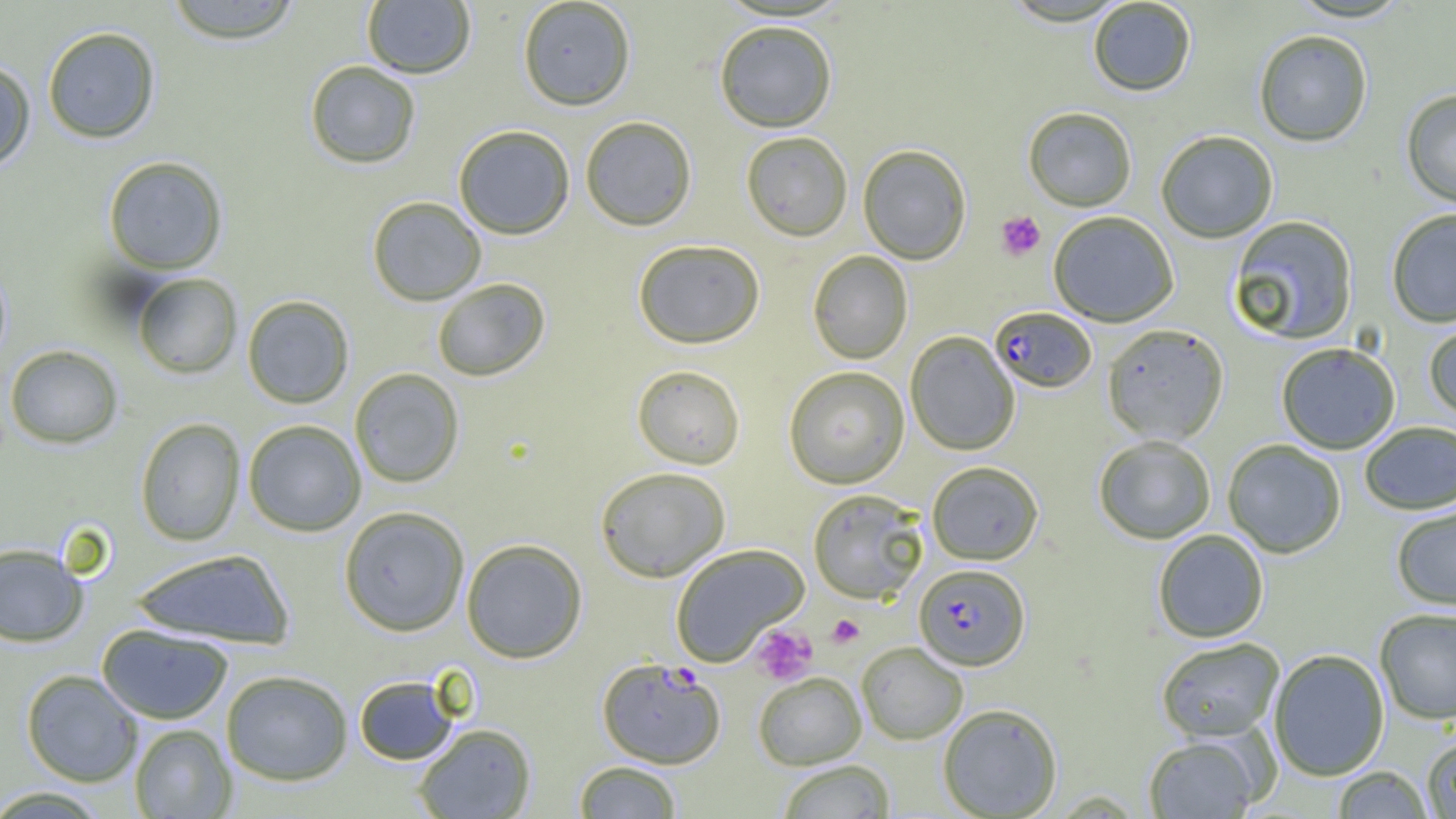

slide_level_diagnosis: Plasmodium falciparum
magnification: 1000x
field_of_view: one of a larger specimen
platelet_locations: 'approximate bounding boxes as (x1, y1, x2, y2) in pixels: (996, 211, 1045, 261), (827, 614, 864, 648), (751, 624, 817, 685)'
plasmodium_falciparum_infected_red_blood_cell_locations: 'approximate bounding boxes as (x1, y1, x2, y2) in pixels: (989, 308, 1097, 394), (914, 564, 1029, 671), (596, 657, 726, 769)'
preparation: thin blood film
image_size: 1456×819 pixels
modality: light microscopy
uninfected_red_blood_cell_locations: 'approximate bounding boxes as (x1, y1, x2, y2) in pixels: (163, 0, 304, 44), (517, 0, 636, 111), (1287, 0, 1412, 24), (362, 1, 476, 79), (1088, 1, 1196, 98), (714, 21, 837, 134), (42, 26, 160, 143), (1254, 31, 1372, 148), (0, 59, 36, 173), (304, 60, 421, 169), (1401, 90, 1456, 210), (1023, 108, 1136, 212), (580, 116, 697, 231), (453, 125, 575, 239), (740, 132, 853, 242), (1156, 132, 1277, 243), (858, 145, 971, 265), (103, 156, 228, 274), (367, 196, 486, 306), (1387, 210, 1456, 328), (1049, 212, 1178, 327), (1228, 216, 1358, 346), (632, 239, 765, 349), (807, 251, 913, 364), (0, 262, 12, 366), (132, 273, 241, 378), (432, 278, 551, 381), (242, 295, 354, 409), (1423, 323, 1456, 421), (1102, 325, 1229, 445), (905, 332, 1020, 456), (4, 344, 123, 448), (1276, 344, 1400, 456), (632, 365, 746, 469), (783, 366, 910, 489), (349, 368, 465, 488), (135, 417, 246, 546), (242, 419, 366, 536), (1360, 422, 1456, 515), (1093, 436, 1215, 545), (1222, 440, 1346, 558), (927, 461, 1043, 565), (595, 466, 731, 582), (807, 489, 929, 604), (338, 505, 470, 636), (1392, 506, 1456, 612), (1153, 530, 1269, 644), (461, 538, 588, 663), (0, 543, 88, 647), (670, 543, 810, 667), (129, 547, 296, 649), (1375, 609, 1456, 725), (96, 623, 233, 724), (1156, 638, 1284, 743), (856, 642, 968, 745), (1269, 650, 1389, 781), (21, 669, 144, 786), (221, 669, 353, 785), (753, 672, 866, 770), (354, 675, 460, 765), (938, 704, 1063, 818), (130, 723, 237, 818), (413, 723, 536, 818), (1144, 736, 1260, 818), (1422, 736, 1456, 818), (777, 760, 895, 819), (573, 761, 682, 818), (1332, 766, 1433, 818), (0, 785, 111, 818)'